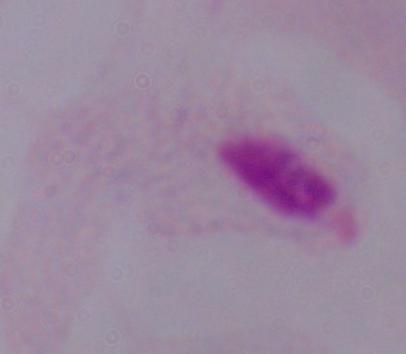

modality = photomicrograph
magnification = 1000x
identification = trichomonad